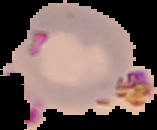
From a thin blood film. Image is 157×130 pixels. Malaria status: parasitized. Cell region segmented out of the field of view; the surrounding area is masked to black.